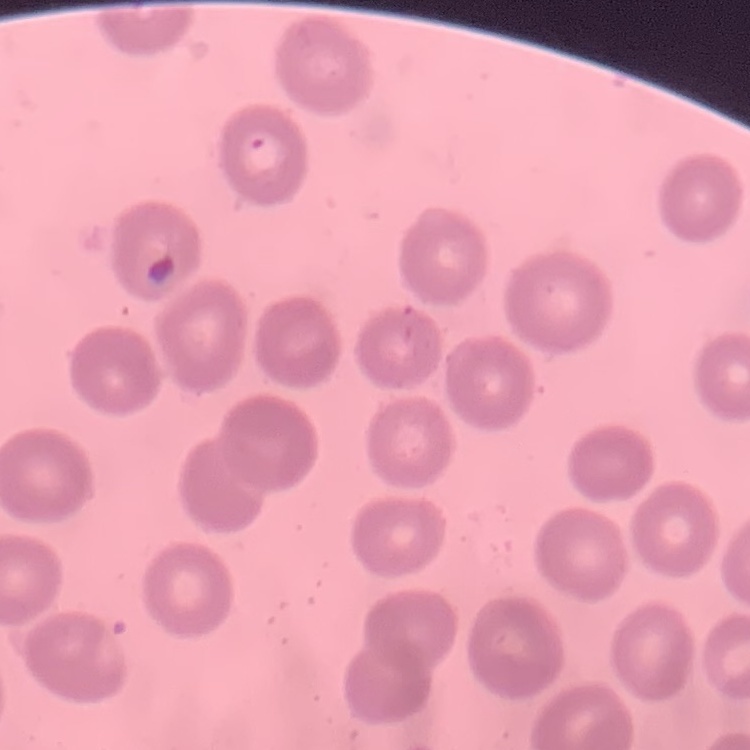
The erythrocytes show no rouleaux formation. Thin blood smear. Stained with either Field's or Giemsa. One tile cut from a larger photomicrograph.